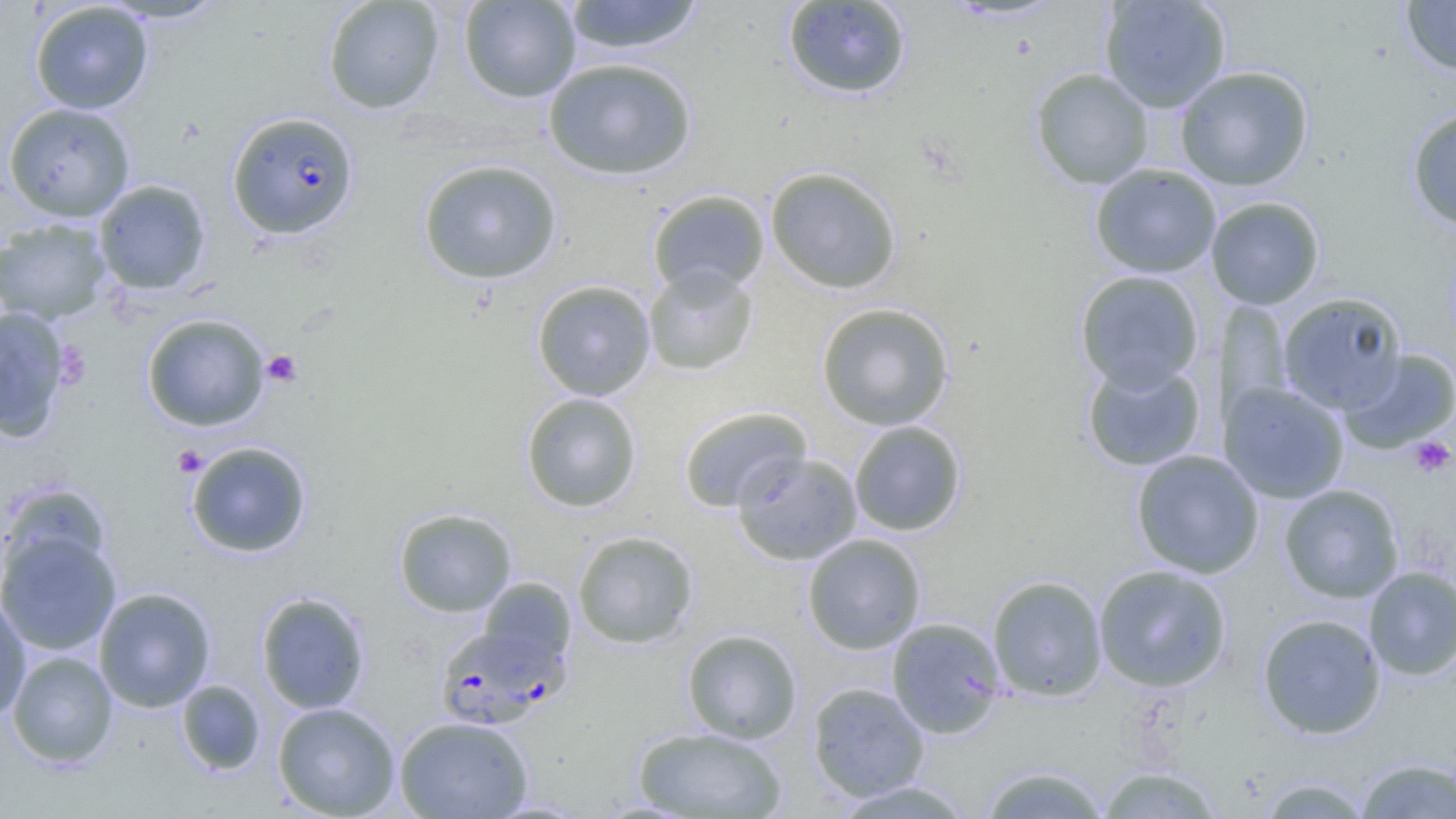

slide-level diagnosis = Plasmodium falciparum
field of view = one of a larger specimen
uninfected red blood cell locations = approximate bounding boxes as (x1, y1, x2, y2) in pixels: (101, 0, 230, 24), (322, 0, 444, 114), (458, 0, 581, 103), (562, 0, 705, 55), (1099, 0, 1231, 112), (1400, 0, 1456, 76), (29, 1, 154, 115), (781, 1, 913, 99), (543, 57, 697, 180), (1174, 65, 1314, 191), (1030, 67, 1154, 190), (3, 102, 136, 222), (1406, 106, 1456, 231), (417, 158, 562, 285), (1089, 163, 1222, 278), (765, 165, 903, 294), (94, 179, 211, 295), (647, 189, 770, 298), (1205, 196, 1326, 310), (0, 218, 112, 325), (643, 265, 758, 377), (1074, 270, 1205, 393), (531, 280, 656, 401), (1277, 292, 1407, 414), (1216, 301, 1294, 423), (815, 302, 955, 431), (0, 305, 72, 444), (141, 313, 270, 432), (1339, 348, 1456, 454), (1081, 358, 1207, 471), (1218, 380, 1350, 504), (521, 392, 642, 512), (678, 406, 812, 513), (849, 420, 967, 536), (185, 441, 312, 558), (1131, 449, 1265, 579), (731, 451, 863, 565), (2, 483, 111, 584), (1279, 484, 1404, 603), (393, 507, 517, 618), (0, 528, 121, 655), (573, 530, 699, 649), (802, 533, 927, 654), (1093, 564, 1232, 692), (1363, 566, 1456, 680), (987, 574, 1108, 702), (476, 577, 578, 675), (93, 586, 216, 713), (256, 591, 371, 715), (0, 597, 31, 724), (1256, 612, 1387, 739), (886, 616, 1006, 739), (682, 628, 802, 744), (7, 650, 118, 769), (176, 679, 266, 775), (807, 681, 930, 803), (272, 701, 402, 818), (394, 715, 533, 818), (633, 726, 789, 818), (1355, 757, 1456, 818), (1094, 763, 1225, 818), (977, 764, 1111, 818), (1256, 776, 1373, 818), (829, 780, 978, 818)
modality = optical microscopy
preparation = thin blood smear
Plasmodium falciparum-infected red blood cell locations = approximate bounding boxes as (x1, y1, x2, y2) in pixels: (226, 110, 360, 241), (434, 624, 567, 730)
platelet locations = approximate bounding boxes as (x1, y1, x2, y2) in pixels: (53, 341, 91, 388), (261, 350, 303, 388), (1409, 436, 1455, 478), (172, 445, 208, 476)
image size = 1456×819 pixels
magnification = 1000x